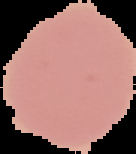

Result: no malaria parasites detected. Cell region segmented out of the field of view; the surrounding area is masked to black. Image is 136×154 pixels. From a thin blood film.